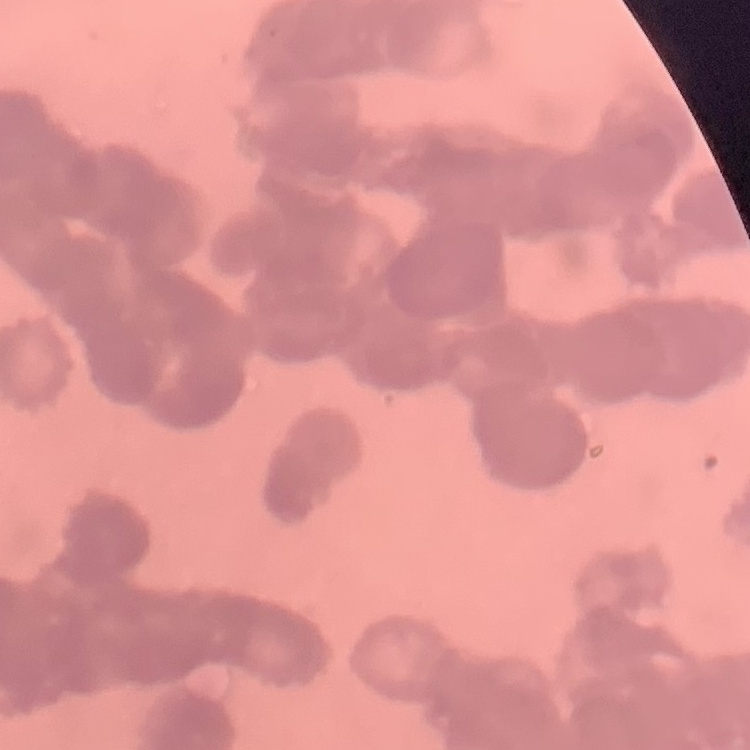
erythrocyte morphology = rouleaux formation
stain = Field's or Giemsa
preparation = thin peripheral smear
image type = square crop of a larger photomicrograph